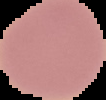
Summary:
  - Result: negative for Plasmodium parasites
  - Image type: cell region segmented out of the field of view; surrounding area masked to black
  - Preparation: thin blood smear
  - Image size: 106×100 pixels